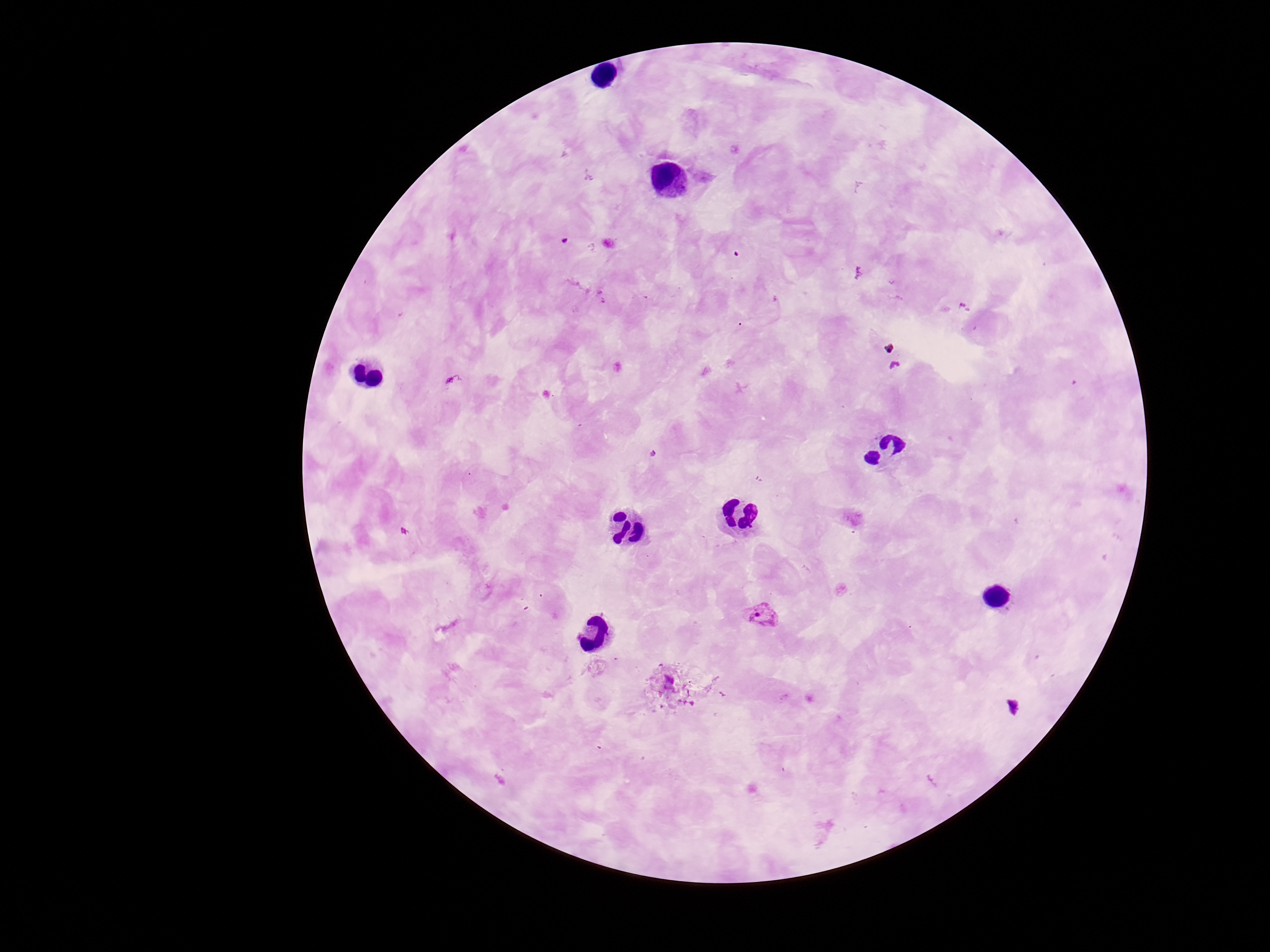

magnification = 100x
Plasmodium parasite locations = approximate centers as {x, y} in pixels: {764, 617}
preparation = thick blood film
field of view = single
patient malaria status = positive
capture = smartphone camera through the microscope eyepiece
image size = 1270×952 pixels
stain = Giemsa